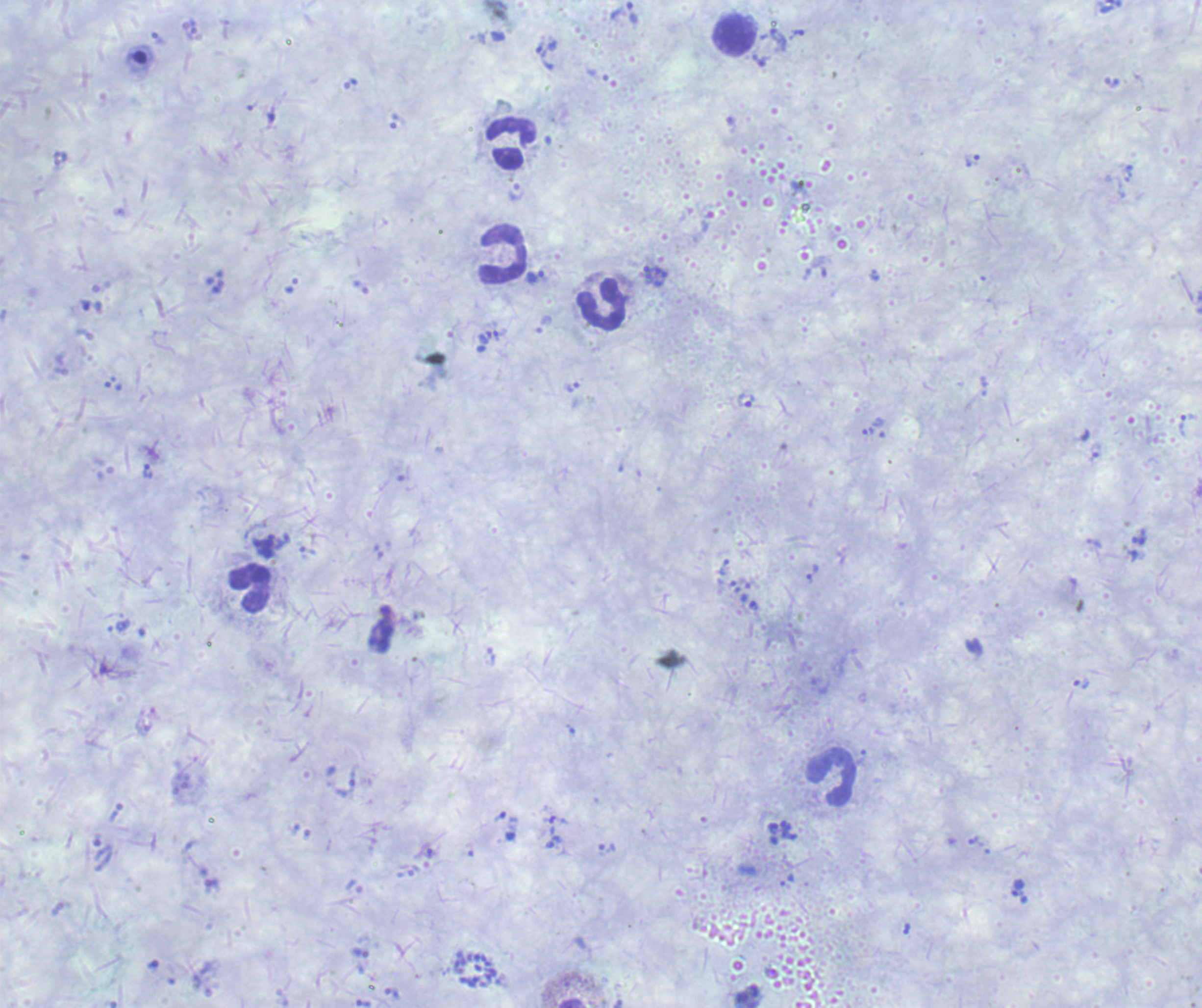

Approximate centers as (x, y) in pixels.
Summary:
  - Trophozoite locations: (632, 14), (546, 55), (972, 161), (535, 278), (572, 387), (746, 402), (867, 432), (147, 472), (810, 573), (1017, 888)
  - Leukocyte locations: (736, 36), (510, 144), (503, 255), (602, 305), (249, 587), (831, 778)
  - Schizont locations: (476, 970)
  - Life-cycle stages observed: trophozoite, schizont
  - Context: previously used in an actual diagnosis
  - Result: positive for malaria parasites
  - Background quality: unsatisfactory
  - Field of view: single
  - Image size: 1202×1008 pixels
  - Magnification: 100x
  - Stain: Romanowsky
  - Preparation: thick smear of blood